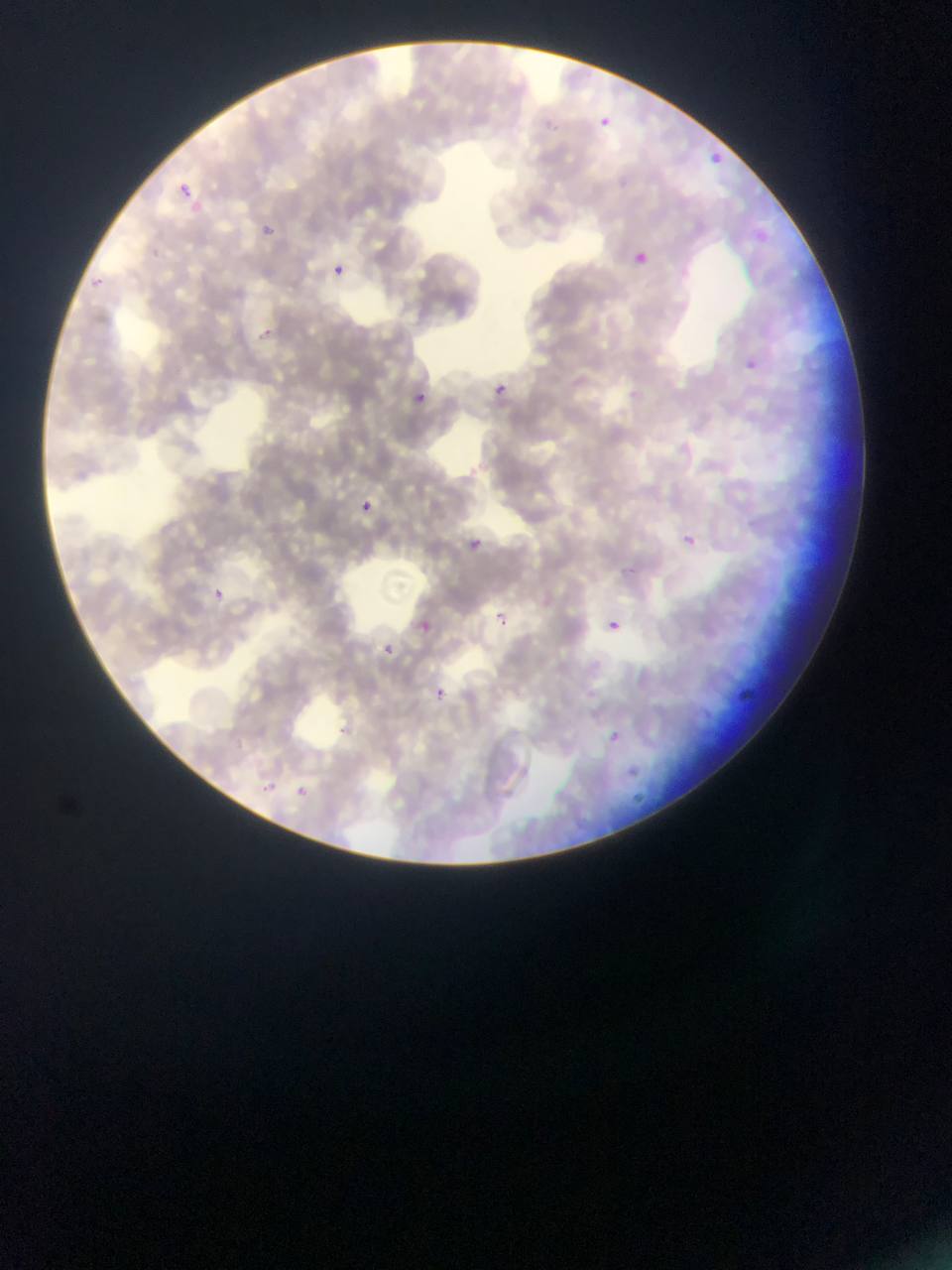

Approximate bounding boxes as (left, top, right, bottom) in pixels. Plasmodium parasite locations: (602, 114, 621, 146), (538, 119, 573, 138), (696, 144, 740, 180), (176, 179, 204, 203), (262, 223, 276, 236), (751, 226, 770, 248), (634, 244, 652, 271), (333, 264, 345, 276), (90, 274, 108, 296), (250, 319, 267, 344), (746, 361, 757, 371), (496, 386, 520, 419), (414, 390, 428, 404), (362, 497, 381, 521), (464, 536, 490, 565), (683, 536, 695, 547), (206, 580, 238, 606), (485, 606, 516, 641), (604, 609, 623, 631), (412, 616, 429, 635), (429, 622, 445, 635), (373, 640, 400, 660), (733, 678, 762, 707), (426, 680, 451, 697), (602, 728, 622, 742), (615, 764, 636, 776), (255, 776, 275, 793), (297, 782, 309, 798), (633, 790, 648, 807). Thin blood film. Image is 952×1270 pixels. Collected in Ghana. One field of view. Photographed through a microscope with a mobile-phone camera.